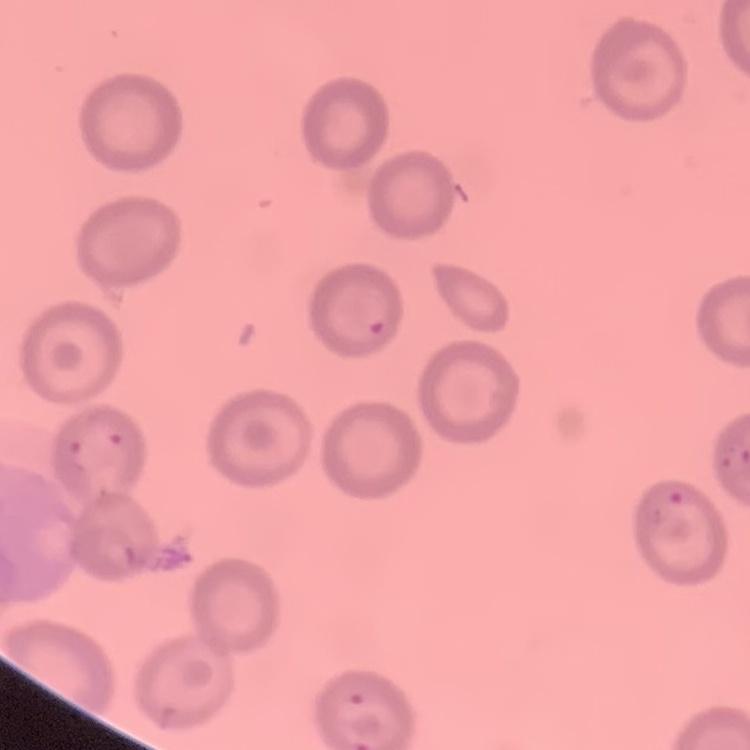

erythrocyte morphology = no rouleaux formation
stain = Field's or Giemsa
preparation = thin blood film
image type = one tile cut from a larger photomicrograph